Point out each Plasmodium parasite and classify it by life-cycle stage.
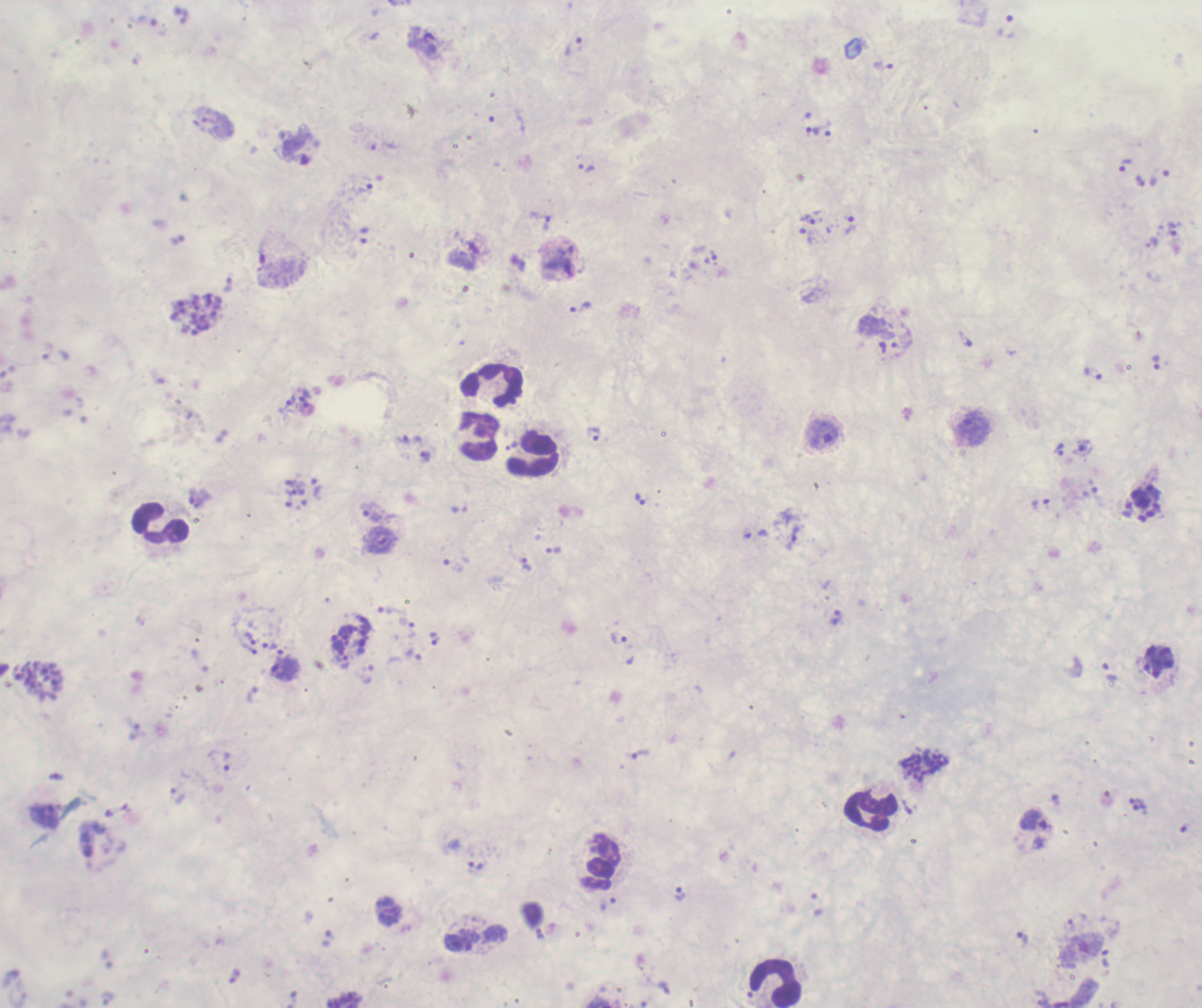

Approximate object centers, in pixels from the top-left corner.
Trophozoites: (x=1006, y=26), (x=574, y=46), (x=884, y=66), (x=813, y=131), (x=295, y=145), (x=1124, y=165), (x=586, y=167), (x=1160, y=178), (x=1141, y=181), (x=809, y=220), (x=546, y=222), (x=849, y=226), (x=1172, y=230), (x=805, y=235), (x=713, y=255), (x=227, y=285), (x=581, y=307), (x=966, y=340), (x=1156, y=363), (x=1093, y=374), (x=286, y=405), (x=823, y=434), (x=594, y=435), (x=409, y=440), (x=1058, y=449), (x=424, y=457), (x=316, y=489), (x=1153, y=492), (x=200, y=498), (x=1140, y=498), (x=289, y=499), (x=641, y=499), (x=1040, y=503), (x=1127, y=510), (x=372, y=511), (x=795, y=533), (x=380, y=540), (x=554, y=551), (x=526, y=565), (x=391, y=610), (x=838, y=618), (x=408, y=623), (x=250, y=637), (x=434, y=638), (x=619, y=638), (x=338, y=644), (x=270, y=645), (x=251, y=650), (x=415, y=656), (x=341, y=658), (x=285, y=669), (x=1110, y=671), (x=368, y=674), (x=253, y=694), (x=641, y=755), (x=228, y=762), (x=178, y=794), (x=1137, y=801), (x=1140, y=808), (x=44, y=816), (x=1033, y=820), (x=476, y=865), (x=680, y=893), (x=607, y=904), (x=817, y=904), (x=539, y=933), (x=1023, y=939), (x=458, y=943), (x=1105, y=958).
Schizonts: (x=196, y=313), (x=38, y=680), (x=926, y=767).
No gametocyte forms observed.

Approximate object centers, in pixels from the top-left corner. Leukocyte locations: (x=492, y=386), (x=479, y=437), (x=533, y=453), (x=161, y=523), (x=870, y=812), (x=602, y=860), (x=776, y=983). One field from this slide. Image is 1202×1008 pixels. Coloration quality: bad. 100x magnification. Romanowsky-stained preparation. Thick smear of blood. Previously used in an actual diagnosis. Background quality: poor.